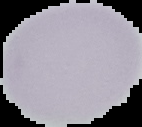

image type = cell region segmented out of the field of view; surrounding area masked to black
image size = 142×127 pixels
result = negative for malaria parasites
preparation = thin blood smear